Report the malaria status of this cell.
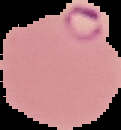

Parasitized.

From a thin blood smear. The area outside the segmented cell region is set to black. Image is 121×130 pixels.